Report the malaria status of this cell.
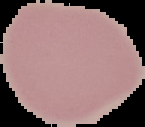
It is uninfected.

Summary:
  - Preparation: thin blood smear
  - Image size: 145×127 pixels
  - Image type: segmented cell region with the area outside set to black